Locate every Plasmodium falciparum-infected red blood cell.
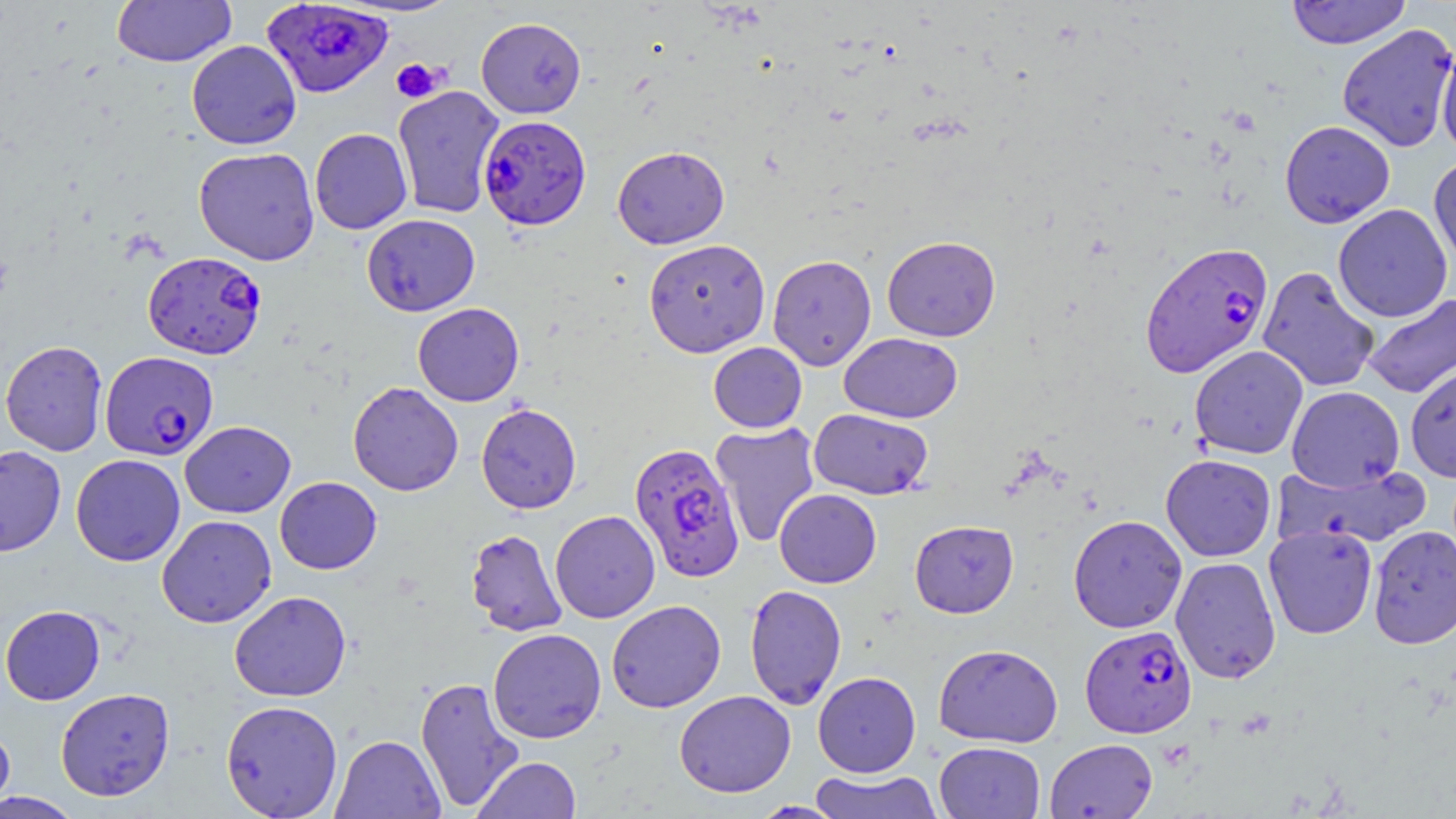
Approximate bounding boxes as (x1, y1, x2, y2) in pixels.
Plasmodium falciparum-infected red blood cells: (261, 1, 393, 100), (478, 115, 592, 231), (1139, 240, 1274, 378), (142, 251, 267, 359), (100, 351, 218, 460), (628, 442, 744, 582), (1080, 625, 1197, 738).

slide-level diagnosis = Plasmodium falciparum
preparation = thin blood film
modality = light microscopy
field of view = one of a larger specimen
stain = May-Grünwald-Giemsa
platelet locations = approximate bounding boxes as (x1, y1, x2, y2) in pixels: (391, 58, 445, 103)
image size = 1456×819 pixels
magnification = 1000x
uninfected red blood cell locations = approximate bounding boxes as (x1, y1, x2, y2) in pixels: (112, 0, 237, 66), (1285, 0, 1412, 49), (476, 16, 586, 118), (1336, 24, 1456, 152), (1436, 36, 1456, 158), (186, 40, 302, 150), (392, 86, 505, 218), (1280, 120, 1395, 228), (309, 128, 412, 234), (194, 146, 320, 266), (612, 146, 729, 249), (1428, 156, 1456, 273), (1333, 204, 1453, 322), (361, 214, 480, 316), (882, 235, 1001, 341), (643, 238, 771, 357), (767, 254, 876, 370), (1258, 266, 1380, 393), (1362, 293, 1456, 398), (413, 303, 524, 406), (839, 332, 963, 423), (1, 340, 108, 456), (708, 342, 807, 433), (1189, 345, 1308, 460), (1405, 364, 1456, 483), (348, 381, 464, 496), (1286, 386, 1404, 491), (476, 403, 581, 514), (809, 408, 933, 499), (179, 420, 296, 518), (710, 422, 821, 548), (0, 445, 66, 557), (71, 454, 186, 566), (1160, 454, 1276, 561), (1272, 462, 1432, 550), (275, 476, 382, 574), (774, 489, 881, 588), (550, 510, 660, 623), (1068, 514, 1187, 633), (156, 515, 276, 628), (909, 520, 1018, 618), (1367, 524, 1456, 649), (1263, 525, 1378, 639), (465, 528, 567, 637), (1171, 556, 1281, 684), (744, 584, 847, 709), (229, 591, 351, 701), (606, 599, 726, 713), (1, 605, 105, 705), (488, 628, 606, 743), (934, 643, 1063, 748), (813, 671, 921, 777), (415, 676, 525, 812), (55, 687, 175, 801), (674, 690, 796, 797), (220, 700, 343, 818), (0, 721, 16, 814), (331, 734, 445, 819), (1044, 738, 1158, 819), (934, 741, 1045, 818), (472, 756, 582, 819), (809, 769, 942, 818), (0, 791, 83, 818), (751, 801, 848, 818)